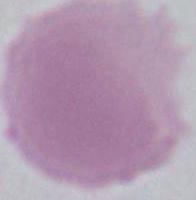
magnification = 1000x
identification = red blood cell
modality = micrograph